Locate every blood parasite and identify its species.
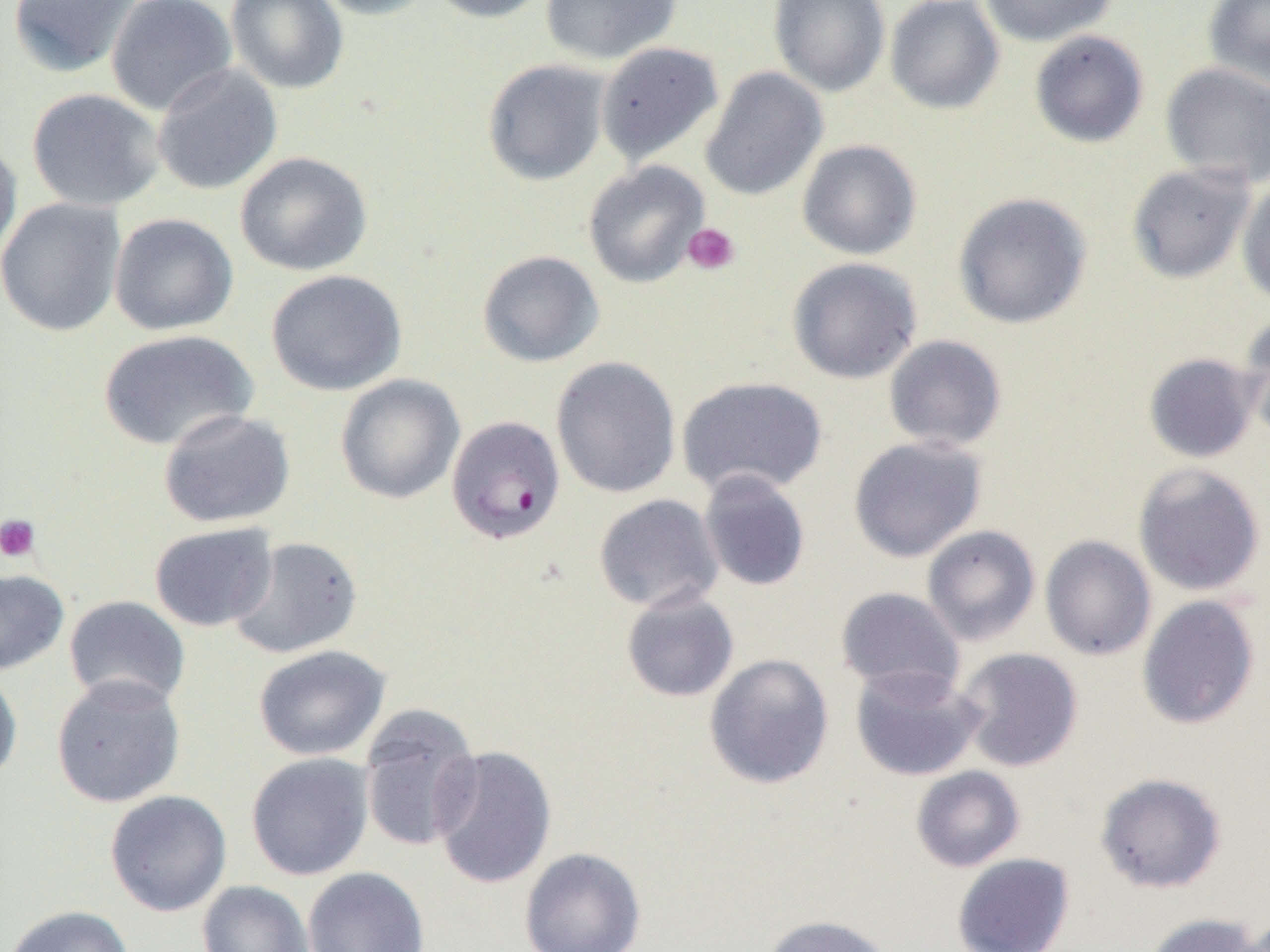
Approximate bounding boxes as [x1, y1, x2, y2] in pixels.
Plasmodium falciparum-infected red blood cells: [446, 415, 566, 545].
No Plasmodium ovale, Plasmodium malariae, Plasmodium vivax, Babesia divergens, or Trypanosoma brucei observed.

slide_level_diagnosis: Plasmodium falciparum
magnification: 1000x
platelet_locations: 'approximate bounding boxes as [x1, y1, x2, y2] in pixels: [683, 222, 740, 276], [0, 513, 41, 562]'
uninfected_red_blood_cell_locations: 'approximate bounding boxes as [x1, y1, x2, y2] in pixels: [7, 0, 141, 78], [105, 0, 237, 116], [225, 0, 349, 94], [310, 0, 440, 20], [423, 0, 552, 23], [540, 0, 682, 65], [768, 0, 891, 98], [885, 0, 1004, 114], [978, 0, 1117, 47], [1202, 0, 1270, 91], [1029, 30, 1149, 148], [595, 42, 724, 165], [482, 59, 611, 186], [1160, 63, 1270, 187], [152, 64, 283, 195], [700, 67, 827, 201], [26, 88, 165, 211], [0, 136, 22, 265], [797, 140, 922, 260], [235, 151, 373, 277], [583, 161, 710, 288], [1126, 162, 1256, 284], [1236, 177, 1270, 308], [952, 191, 1093, 330], [0, 197, 126, 337], [108, 213, 239, 336], [477, 250, 605, 368], [787, 257, 923, 384], [265, 269, 407, 396], [1236, 310, 1270, 440], [96, 329, 259, 453], [883, 334, 1007, 452], [1143, 353, 1260, 463], [551, 356, 681, 498], [334, 374, 465, 504], [676, 376, 828, 498], [158, 408, 295, 528], [848, 436, 987, 562], [1133, 462, 1266, 597], [698, 471, 811, 592], [593, 494, 724, 613], [149, 522, 278, 632], [921, 524, 1041, 646], [1040, 535, 1156, 661], [229, 536, 362, 659], [0, 568, 70, 676], [835, 586, 965, 700], [620, 589, 740, 703], [63, 595, 191, 709], [1136, 595, 1260, 730], [253, 645, 390, 761], [954, 647, 1083, 772], [704, 653, 834, 790], [849, 666, 984, 782], [0, 667, 22, 786], [51, 674, 186, 807], [358, 704, 483, 853], [430, 745, 557, 890], [246, 752, 374, 881], [910, 765, 1026, 872], [1095, 772, 1227, 894], [105, 790, 232, 917], [519, 847, 646, 952], [951, 853, 1075, 952], [303, 866, 430, 952], [197, 880, 314, 952], [3, 905, 134, 952], [1143, 912, 1265, 952], [760, 914, 893, 952], [1234, 914, 1270, 952]'
field_of_view: single
preparation: thin blood film
image_size: 1270×952 pixels
modality: light microscopy